Give the extent of all uninfected red blood cells.
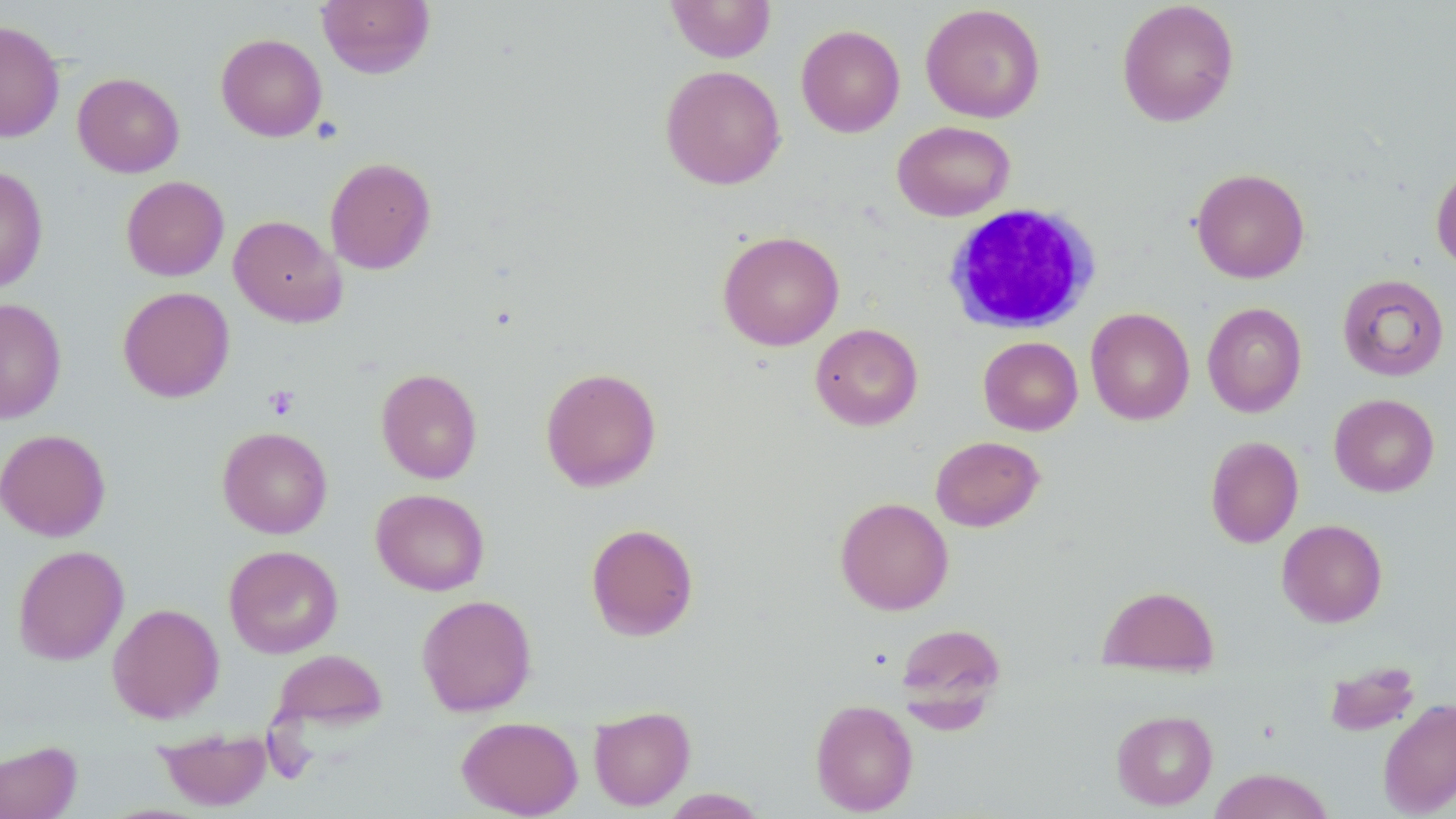
Approximate bounding boxes as [x1, y1, x2, y2] in pixels.
Uninfected red blood cells: [316, 0, 436, 79], [666, 0, 776, 62], [1116, 1, 1240, 127], [920, 4, 1045, 123], [0, 20, 65, 143], [796, 24, 905, 137], [216, 33, 327, 142], [660, 65, 786, 189], [73, 72, 184, 177], [892, 120, 1016, 221], [325, 157, 436, 274], [1431, 162, 1456, 271], [0, 166, 49, 294], [1192, 168, 1310, 283], [121, 176, 229, 281], [228, 214, 345, 327], [717, 230, 845, 351], [1337, 273, 1449, 381], [117, 286, 235, 403], [0, 297, 67, 423], [1202, 302, 1307, 417], [1086, 307, 1194, 425], [810, 323, 923, 431], [978, 336, 1083, 435], [540, 367, 661, 492], [376, 368, 483, 484], [1329, 394, 1439, 497], [217, 426, 333, 538], [0, 429, 111, 541], [930, 435, 1045, 532], [1205, 435, 1304, 548], [371, 489, 490, 596], [835, 496, 953, 615], [1277, 519, 1387, 627], [585, 522, 699, 641], [12, 544, 129, 665], [223, 544, 344, 659], [1097, 585, 1219, 676], [416, 594, 537, 716], [107, 603, 224, 723], [894, 621, 1006, 722], [272, 649, 388, 733], [1325, 660, 1421, 736], [810, 698, 918, 815], [1378, 698, 1456, 817], [589, 705, 695, 810], [1111, 710, 1217, 810], [456, 716, 583, 818], [155, 727, 272, 811], [0, 740, 82, 819], [1208, 768, 1335, 819], [661, 789, 767, 818].

slide-level diagnosis = no evidence of blood parasites
white blood cell locations = approximate bounding boxes as [x1, y1, x2, y2] in pixels: [944, 202, 1101, 334]
field of view = single
platelet locations = approximate bounding boxes as [x1, y1, x2, y2] in pixels: [263, 385, 301, 420]
image size = 1456×819 pixels
modality = optical microscopy
stain = May-Grünwald-Giemsa
preparation = thin blood smear
magnification = 1000x